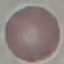

Result: no malaria parasites detected. Thin blood smear. Cell patch, automatically extracted from a larger field of view and resized to 64 × 64 pixels. Photographed with a smartphone camera at the microscope eyepiece. Giemsa stain.